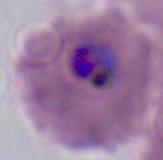
400x or 1000x magnification. A Plasmodium parasite is shown. Micrograph.